Locate and identify every blood parasite.
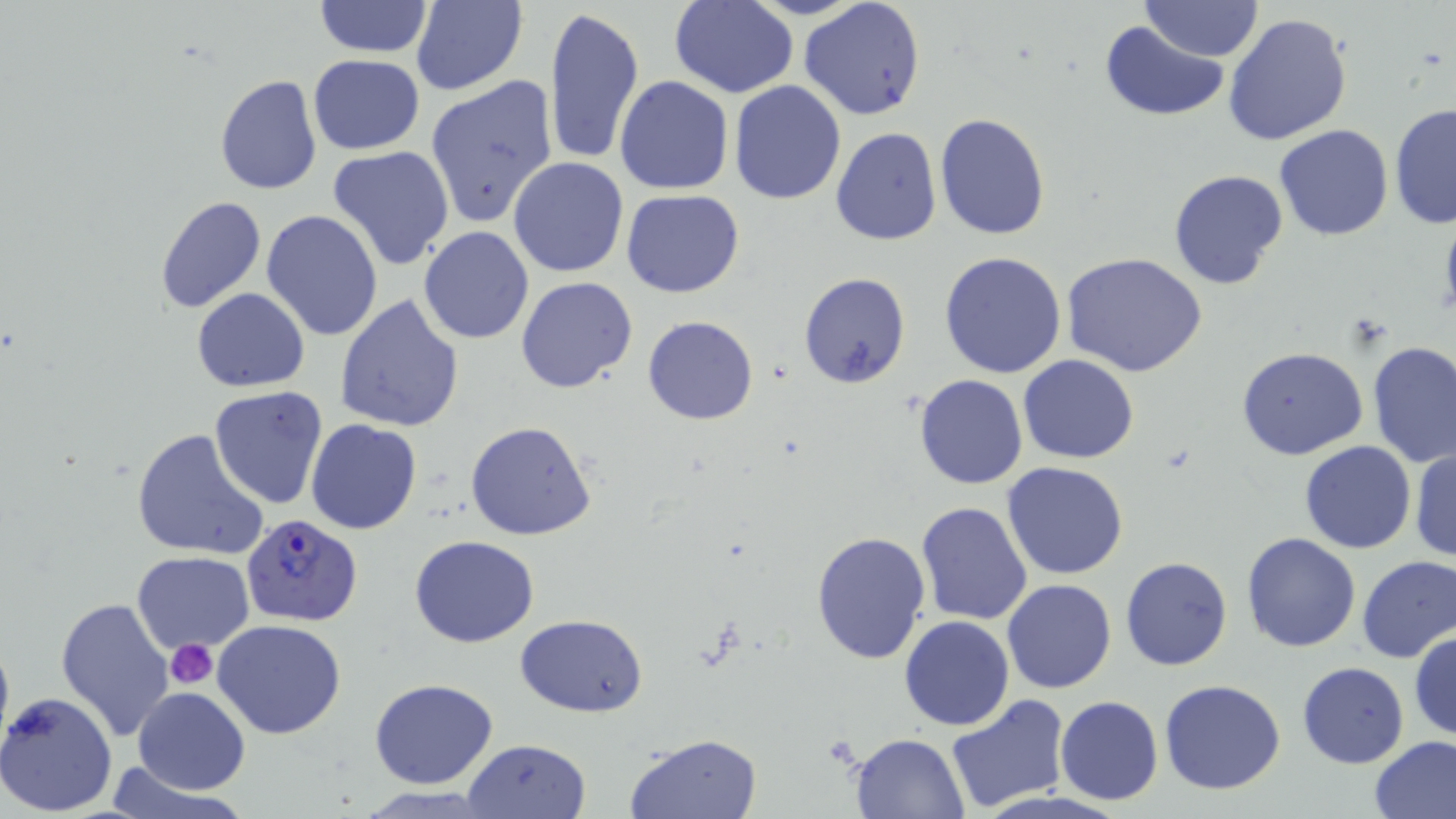

Approximate bounding boxes as (x1, y1, x2, y2) in pixels.
Plasmodium falciparum-infected red blood cells: (241, 514, 361, 626).
No Plasmodium ovale, Plasmodium malariae, Plasmodium vivax, Babesia divergens, or Trypanosoma brucei observed.

Platelet locations: (166, 638, 220, 687). Uninfected red blood cell locations: (312, 0, 434, 58), (670, 0, 799, 99), (799, 0, 927, 121), (1141, 0, 1263, 61), (411, 1, 528, 96), (545, 4, 645, 169), (1223, 12, 1353, 146), (1101, 21, 1228, 121), (308, 55, 425, 155), (215, 74, 322, 194), (425, 74, 560, 230), (614, 74, 734, 197), (729, 80, 847, 204), (1390, 102, 1456, 232), (933, 114, 1051, 241), (1273, 124, 1394, 241), (830, 127, 941, 246), (327, 144, 455, 270), (508, 156, 630, 277), (1169, 169, 1289, 292), (622, 189, 745, 298), (155, 195, 266, 314), (262, 210, 382, 341), (419, 226, 535, 344), (940, 251, 1069, 378), (1063, 252, 1209, 376), (800, 271, 912, 390), (515, 275, 638, 394), (192, 289, 311, 392), (334, 294, 466, 433), (643, 315, 758, 424), (1366, 341, 1455, 468), (1236, 346, 1368, 459), (1018, 355, 1137, 463), (914, 374, 1028, 490), (210, 386, 329, 508), (305, 419, 422, 536), (465, 420, 597, 541), (132, 426, 272, 562), (1299, 440, 1416, 554), (1409, 445, 1455, 562), (1002, 462, 1130, 581), (915, 501, 1033, 625), (810, 517, 1031, 642), (810, 529, 929, 666), (1241, 532, 1362, 653), (407, 534, 541, 648), (132, 553, 255, 652), (1357, 555, 1455, 663), (1121, 557, 1233, 671), (1002, 578, 1116, 694), (57, 597, 177, 741), (516, 613, 648, 717), (899, 615, 1014, 731), (213, 619, 346, 739), (1409, 628, 1456, 742), (1297, 661, 1409, 767), (369, 678, 497, 789), (1158, 680, 1286, 795), (133, 687, 251, 794), (0, 689, 118, 817), (944, 694, 1073, 810), (1055, 696, 1163, 805), (849, 731, 968, 815), (626, 732, 763, 819), (1368, 737, 1456, 818), (462, 738, 591, 819), (104, 764, 240, 817), (353, 787, 503, 818). Slide-level diagnosis: Plasmodium falciparum. May-Grünwald-Giemsa stain. Image is 1456×819 pixels. 1000x magnification. Light microscopy. One field of a larger specimen. Thin blood film.